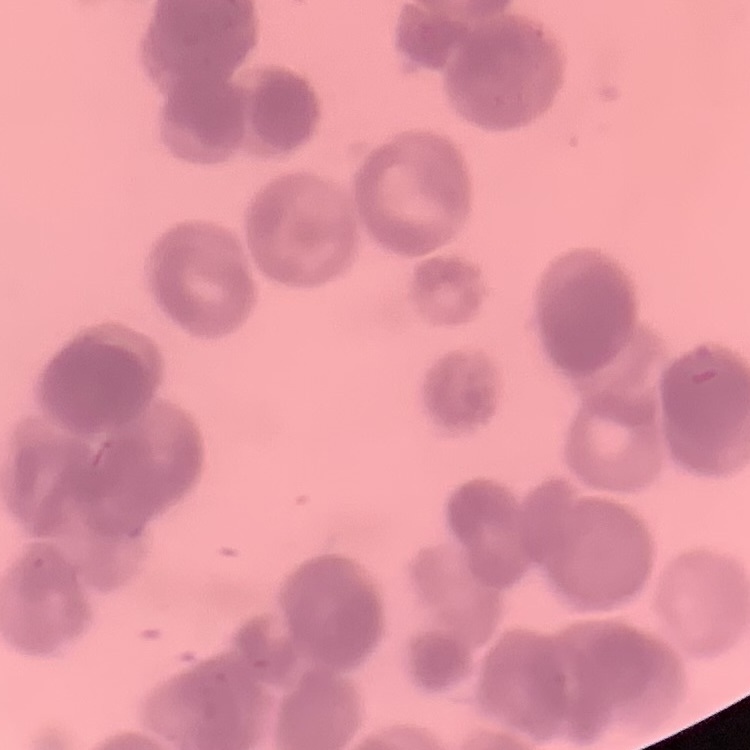

Summary:
  - Red blood cell morphology: rouleaux formation
  - Image type: one tile cut from a larger photomicrograph
  - Stain: Field's or Giemsa
  - Preparation: thin blood film